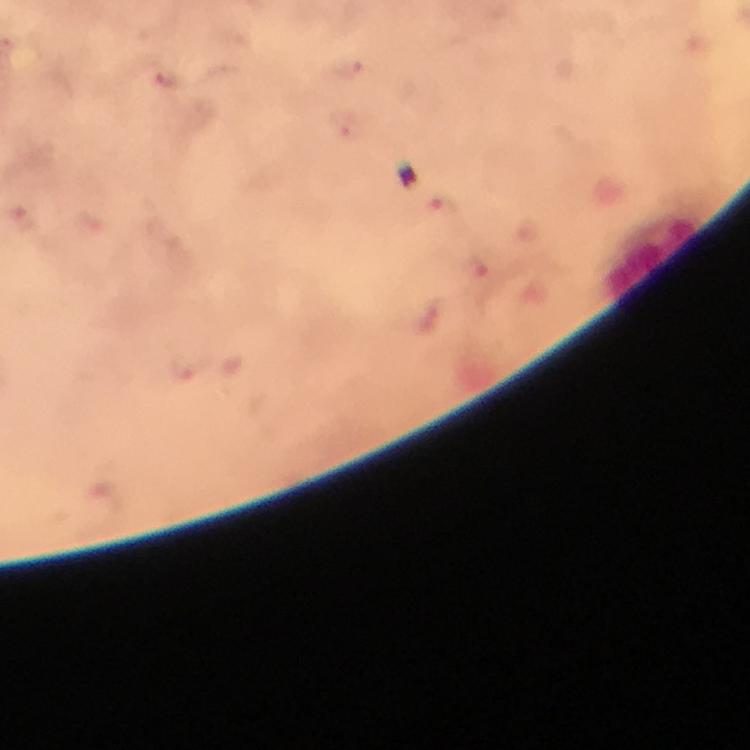 Approximate centers as (x, y) in pixels. Leukocyte locations: (655, 245). Plasmodium parasite locations: (352, 67), (168, 74), (345, 125), (477, 269). Immersion oil was used. At 100x magnification. Giemsa stain. A crop from one field of view. Image is 750×750 pixels. From a diagnostic examination for malaria. Photographed through the microscope with a smartphone camera. Thick blood film.